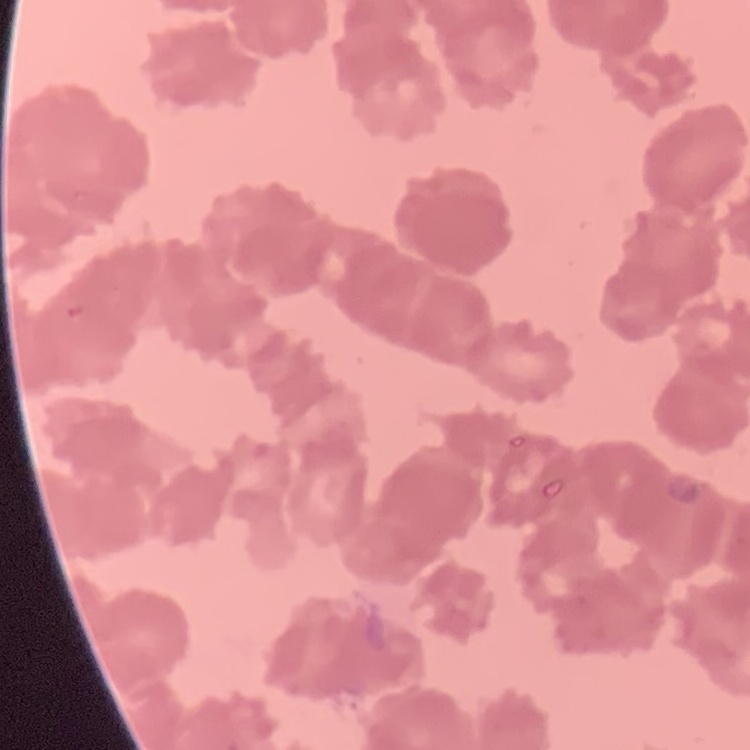
The erythrocytes show rouleaux formation. Thin blood film. One tile cut from a larger photomicrograph. Field's or Giemsa stain.